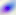 Toxoplasma gondii is shown. 400x magnification. Micrograph.